Identify the blood parasite species.
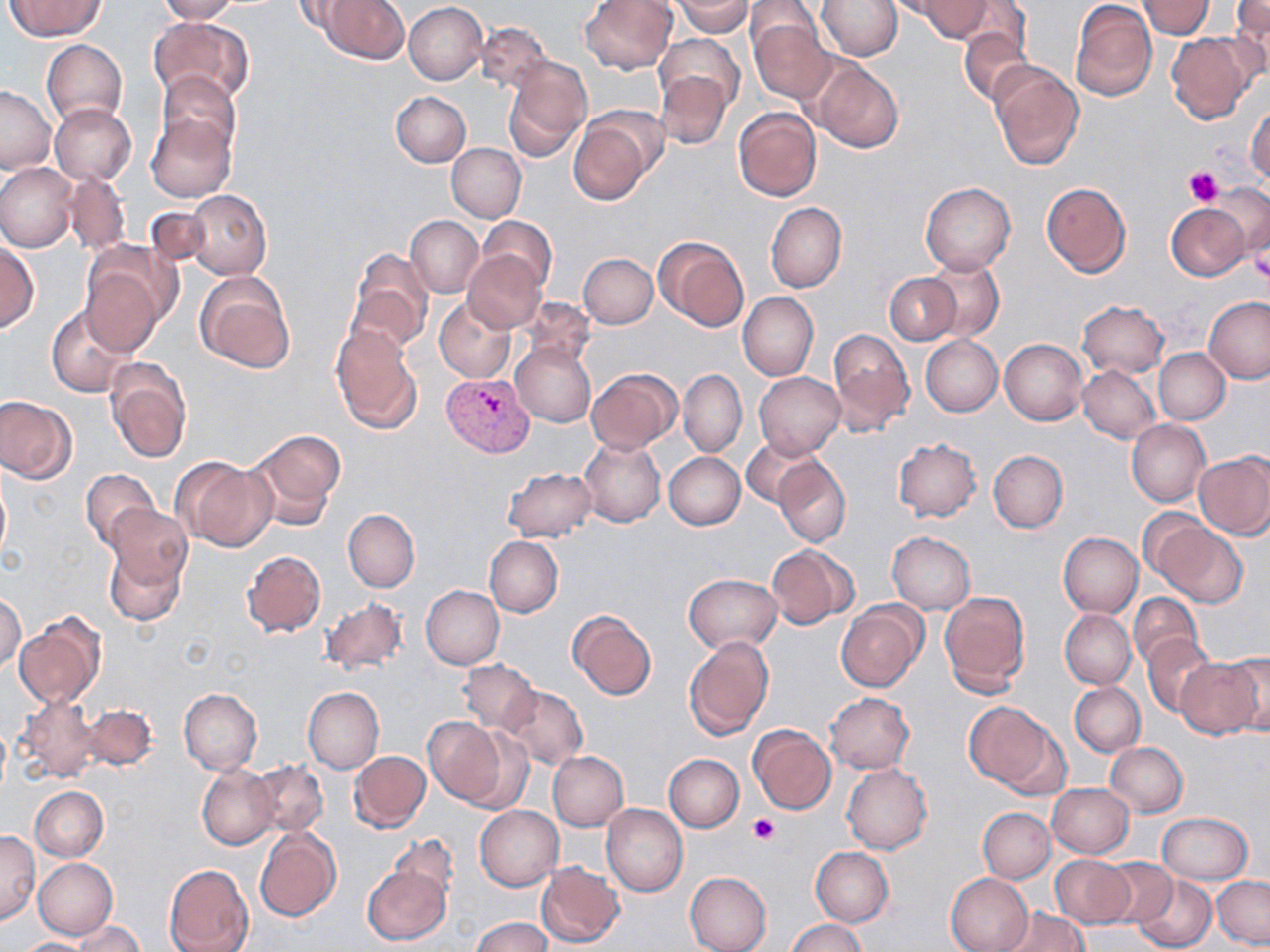
Plasmodium vivax.

platelet locations = approximate bounding boxes as (x1,y1)-(x2,y2) corner pairs in pixels: (1184,165)-(1224,205), (1249,248)-(1270,285), (747,812)-(780,846)
uninfected red blood cell locations = approximate bounding boxes as (x1,y1)-(x2,y2) corner pairs in pixels: (4,0)-(106,39), (155,0)-(238,23), (294,0)-(362,37), (322,0)-(409,64), (579,0)-(678,75), (675,0)-(753,37), (885,0)-(968,21), (912,0)-(996,41), (1070,0)-(1157,101), (1138,0)-(1215,38), (816,1)-(902,61), (1228,1)-(1270,79), (403,2)-(487,84), (743,3)-(823,63), (749,15)-(835,103), (148,17)-(253,105), (475,22)-(550,94), (959,25)-(1035,106), (1166,31)-(1256,123), (656,34)-(744,114), (41,39)-(126,127), (503,56)-(592,161), (808,58)-(904,153), (988,61)-(1084,170), (157,70)-(240,157), (654,71)-(733,148), (0,86)-(55,173), (391,91)-(471,166), (49,103)-(136,186), (1246,104)-(1270,185), (733,107)-(822,202), (147,112)-(237,202), (568,115)-(654,205), (447,143)-(526,222), (0,162)-(79,252), (62,172)-(131,256), (920,181)-(1016,274), (1040,182)-(1131,277), (1205,183)-(1270,258), (186,189)-(271,279), (766,202)-(846,293), (1166,203)-(1252,281), (145,205)-(212,268), (405,215)-(483,298), (476,217)-(557,293), (654,236)-(749,332), (0,243)-(39,331), (346,249)-(433,352), (463,249)-(546,332), (578,253)-(657,329), (922,256)-(1005,342), (79,263)-(165,357), (195,272)-(296,374), (884,273)-(961,345), (737,292)-(818,382), (520,297)-(594,370), (1204,297)-(1270,384), (434,299)-(518,383), (1077,301)-(1169,378), (47,305)-(136,398), (330,325)-(421,433), (827,328)-(914,435), (921,335)-(1003,416), (999,339)-(1088,424), (510,343)-(595,428), (1154,348)-(1231,425), (106,359)-(192,463), (1077,365)-(1162,444), (585,368)-(681,453), (678,370)-(746,457), (754,372)-(844,461), (0,396)-(76,483), (1126,419)-(1211,507), (245,429)-(345,527), (579,437)-(665,527), (892,437)-(982,522), (741,438)-(822,508), (988,449)-(1068,533), (664,451)-(745,530), (1194,453)-(1270,540), (773,454)-(851,548), (171,458)-(275,551), (503,467)-(597,541), (80,468)-(160,551), (0,472)-(10,567), (106,504)-(191,590), (1137,508)-(1212,581), (343,510)-(419,592), (1152,522)-(1247,608), (887,532)-(976,614), (1058,532)-(1143,617), (484,536)-(563,617), (103,539)-(186,627), (766,543)-(857,628), (241,549)-(325,636), (684,574)-(781,654), (422,586)-(504,670), (939,590)-(1031,696), (1,593)-(26,674), (1128,593)-(1204,670), (320,597)-(409,675), (835,600)-(928,693), (567,609)-(657,700), (1060,609)-(1135,688), (14,618)-(103,708), (1141,632)-(1217,717), (682,635)-(773,741), (1222,653)-(1270,735), (1174,657)-(1264,738), (458,660)-(540,733), (1069,683)-(1145,757), (499,685)-(587,769), (303,687)-(384,774), (179,688)-(262,775), (825,692)-(914,773), (15,693)-(101,783), (964,701)-(1062,793), (82,703)-(158,770), (422,717)-(508,806), (747,726)-(836,814), (460,729)-(533,812), (1106,742)-(1187,817), (348,751)-(431,833), (548,751)-(628,830), (663,753)-(744,831), (250,760)-(328,837), (197,763)-(277,851), (842,763)-(932,854), (1046,783)-(1133,858), (30,786)-(107,861), (601,804)-(688,896), (475,805)-(563,890), (978,808)-(1055,883), (1156,812)-(1252,885), (255,828)-(341,921), (0,830)-(40,923), (390,834)-(460,905), (811,846)-(893,926), (1051,855)-(1132,926), (33,858)-(118,939), (1099,858)-(1177,929), (535,861)-(624,947), (362,862)-(452,946), (164,864)-(253,952), (684,872)-(771,952), (945,872)-(1033,952), (1130,875)-(1216,952), (1212,876)-(1270,949), (998,907)-(1090,952), (470,916)-(552,952), (785,918)-(868,952), (73,922)-(144,952), (14,937)-(96,952)
preparation = thin blood smear
image size = 1270×952 pixels
field of view = single
magnification = 1000x
Plasmodium vivax-infected red blood cell locations = approximate bounding boxes as (x1,y1)-(x2,y2) corner pairs in pixels: (444,370)-(535,456)
modality = light microscopy
stain = May-Grünwald-Giemsa